Locate every Babesia divergens-infected red blood cell.
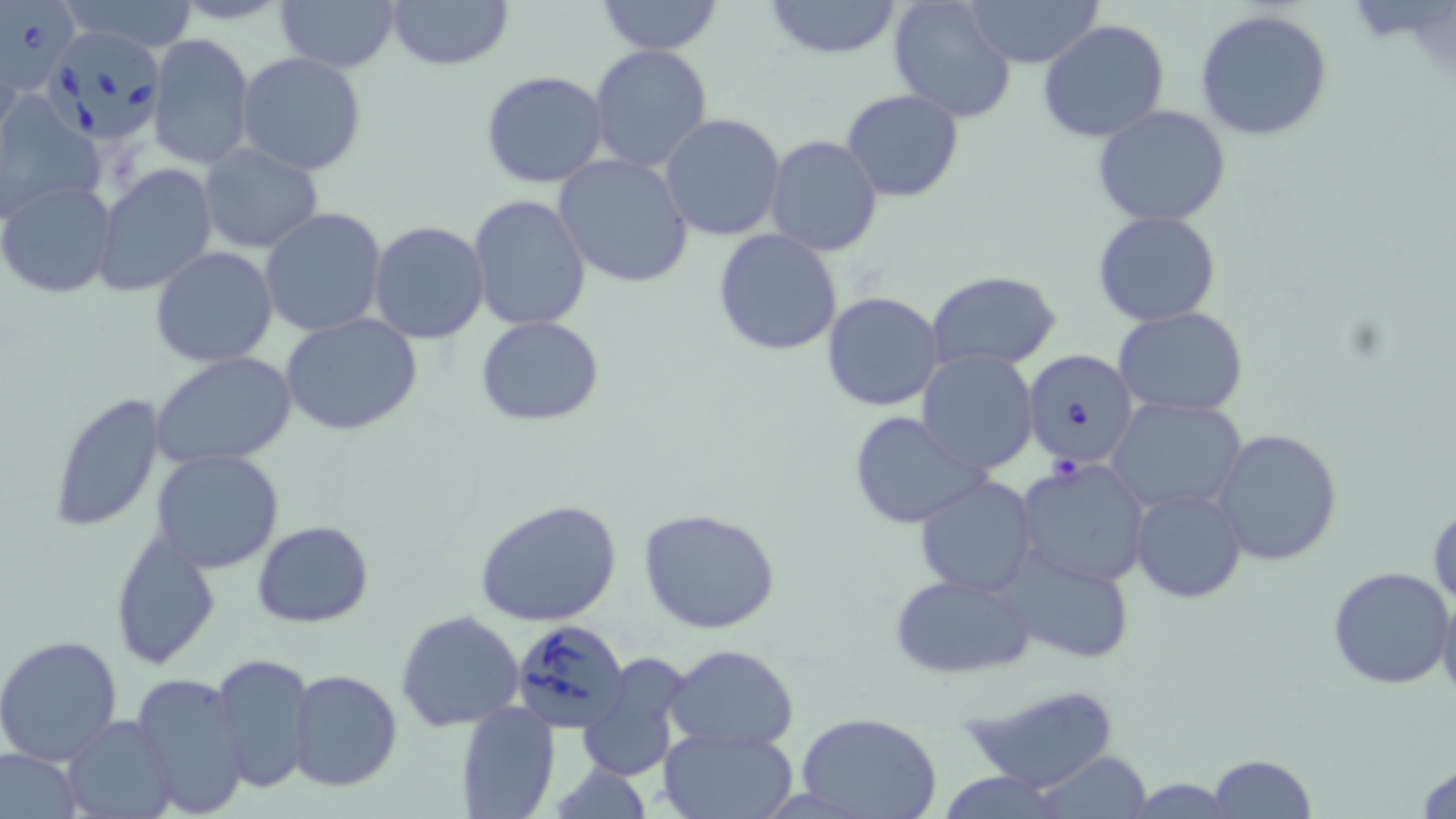

Approximate bounding boxes as (x1,y1)-(x2,y2) corner pairs in pixels.
Babesia divergens-infected red blood cells: (0,0)-(87,105), (48,31)-(177,146), (1024,350)-(1140,472), (511,619)-(628,735).

Summary:
  - Uninfected red blood cell locations: (60,0)-(203,52), (276,0)-(400,73), (385,0)-(513,70), (597,0)-(722,55), (888,0)-(1018,121), (963,0)-(1104,67), (761,1)-(904,58), (1195,8)-(1334,141), (1037,19)-(1170,143), (146,34)-(255,169), (588,45)-(713,174), (235,51)-(368,175), (479,71)-(610,190), (842,88)-(963,202), (0,92)-(104,222), (1093,106)-(1233,227), (659,114)-(787,241), (766,134)-(883,258), (198,142)-(324,255), (553,154)-(695,287), (95,163)-(218,298), (0,180)-(119,300), (468,195)-(591,332), (260,207)-(385,338), (1094,210)-(1222,327), (369,221)-(490,344), (714,229)-(842,356), (151,246)-(277,367), (927,271)-(1063,372), (821,291)-(946,411), (1115,306)-(1247,419), (281,314)-(424,436), (475,316)-(605,425), (916,350)-(1039,474), (151,351)-(298,469), (48,391)-(166,533), (1107,396)-(1248,515), (849,411)-(989,529), (1212,426)-(1345,568), (151,449)-(286,574), (1015,457)-(1151,589), (915,475)-(1039,594), (1131,486)-(1247,604), (475,497)-(624,627), (1429,504)-(1455,609), (639,506)-(781,634), (252,521)-(373,628), (110,530)-(221,670), (997,547)-(1135,665), (1327,565)-(1456,689), (888,572)-(1037,679), (1437,589)-(1456,706), (396,608)-(526,733), (0,634)-(123,766), (666,643)-(799,748), (213,650)-(317,794), (576,655)-(693,783), (131,670)-(249,817), (287,670)-(403,791), (962,684)-(1125,792), (457,703)-(561,819), (796,712)-(943,819), (64,714)-(177,817), (659,726)-(798,818), (0,747)-(83,819), (1031,749)-(1155,818), (1207,754)-(1314,818), (1415,759)-(1456,817), (936,772)-(1069,817), (1123,778)-(1239,814)
  - Slide-level diagnosis: Babesia divergens
  - Field of view: single
  - Stain: May-Grünwald-Giemsa
  - Preparation: thin blood smear
  - Modality: optical microscopy
  - Magnification: 1000x
  - Image size: 1456×819 pixels